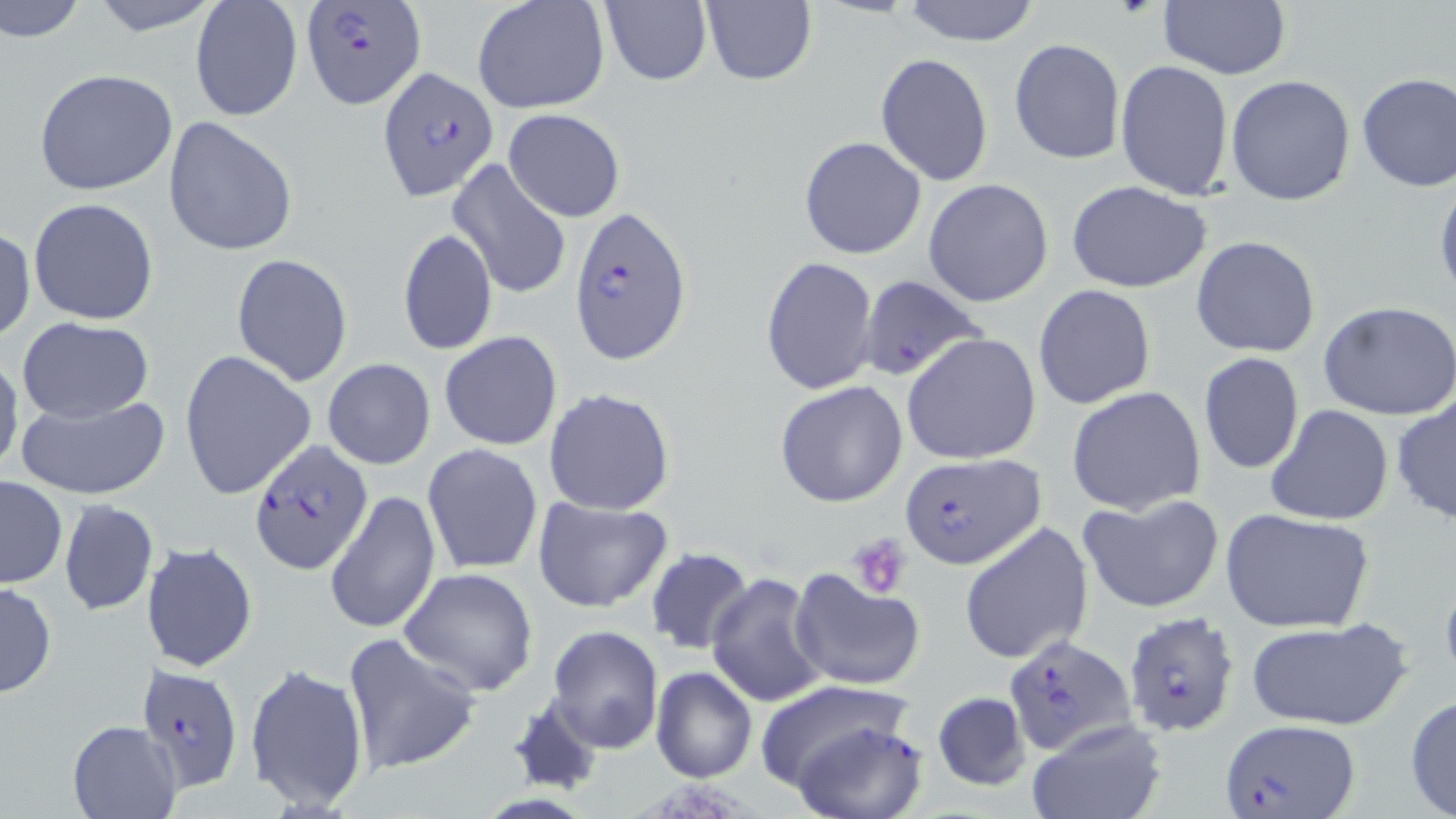

Summary:
  - Coordinate format: approximate bounding boxes as [x1, y1, x2, y2] in pixels
  - Uninfected red blood cell locations: [85, 0, 226, 35], [472, 0, 611, 115], [600, 0, 712, 87], [700, 0, 817, 87], [1159, 0, 1291, 81], [1, 1, 90, 46], [900, 1, 1043, 46], [190, 3, 301, 121], [1008, 38, 1125, 165], [875, 53, 993, 185], [1115, 59, 1234, 199], [34, 68, 180, 197], [1356, 72, 1455, 193], [1226, 75, 1357, 208], [503, 109, 624, 222], [163, 116, 297, 257], [798, 136, 926, 260], [446, 159, 574, 301], [1435, 176, 1456, 309], [923, 178, 1054, 305], [1067, 180, 1212, 293], [28, 197, 159, 324], [0, 227, 35, 344], [399, 228, 497, 356], [1191, 235, 1322, 357], [231, 253, 354, 387], [760, 256, 880, 398], [1032, 284, 1157, 410], [1320, 301, 1456, 421], [15, 316, 156, 422], [440, 332, 563, 450], [901, 332, 1043, 465], [0, 350, 23, 482], [178, 350, 317, 500], [1198, 352, 1304, 474], [322, 358, 436, 469], [774, 379, 908, 508], [1067, 386, 1206, 516], [543, 387, 676, 515], [14, 393, 170, 499], [1390, 393, 1455, 527], [1266, 404, 1394, 528], [422, 443, 543, 574], [0, 477, 67, 589], [324, 489, 441, 635], [1077, 493, 1224, 614], [531, 496, 673, 613], [57, 499, 159, 615], [1219, 508, 1374, 634], [958, 521, 1094, 666], [140, 541, 259, 672], [645, 547, 754, 656], [398, 567, 539, 695], [787, 567, 925, 691], [705, 570, 831, 708], [0, 581, 56, 699], [1244, 618, 1412, 731], [546, 625, 665, 754], [341, 633, 481, 775], [244, 662, 370, 812], [650, 667, 757, 783], [754, 678, 915, 796], [931, 690, 1033, 793], [1405, 695, 1456, 818], [785, 718, 930, 819], [66, 720, 180, 818], [1023, 720, 1169, 819]
  - Platelet locations: [844, 534, 912, 599]
  - Plasmodium falciparum-infected red blood cell locations: [300, 1, 427, 109], [377, 66, 499, 201], [569, 206, 694, 364], [858, 275, 989, 384], [248, 439, 371, 574], [898, 452, 1044, 570], [1121, 611, 1244, 739], [1005, 634, 1137, 757], [136, 663, 243, 795], [1222, 717, 1358, 819]
  - Slide-level diagnosis: Plasmodium falciparum
  - Stain: May-Grünwald-Giemsa
  - Magnification: 1000x
  - Modality: optical microscopy
  - Preparation: thin blood film
  - Image size: 1456×819 pixels
  - Field of view: one of a larger specimen